Report the malaria status of this cell.
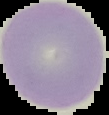
Uninfected.

preparation = thin blood smear
image type = segmented cell region on a black background
image size = 109×115 pixels